Locate every Plasmodium parasite.
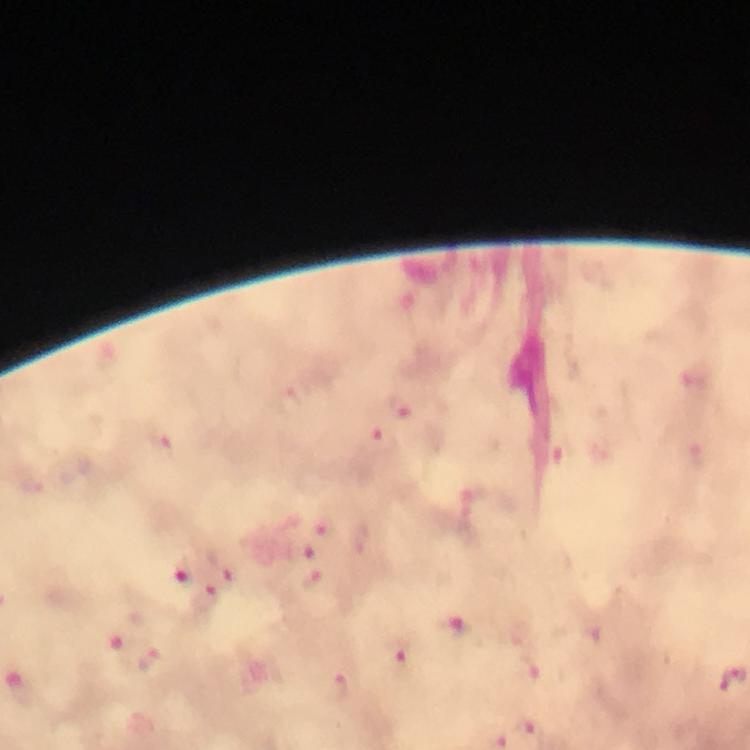

Approximate centers as {x, y} in pixels.
Plasmodium parasites: {293, 405}, {402, 408}, {383, 441}, {164, 449}, {564, 455}, {699, 456}, {324, 523}, {300, 550}, {226, 563}, {182, 570}, {311, 584}, {206, 599}, {461, 630}, {519, 634}, {590, 640}, {395, 654}, {150, 660}, {530, 677}, {333, 688}, {528, 728}.

Summary:
  - Image size: 750×750 pixels
  - Magnification: 100x
  - Context: from a malaria diagnostic workup
  - Capture: smartphone mounted on the microscope
  - Cropped from: one field of view
  - Stain: Giemsa
  - Immersion oil: applied
  - Preparation: thick blood film